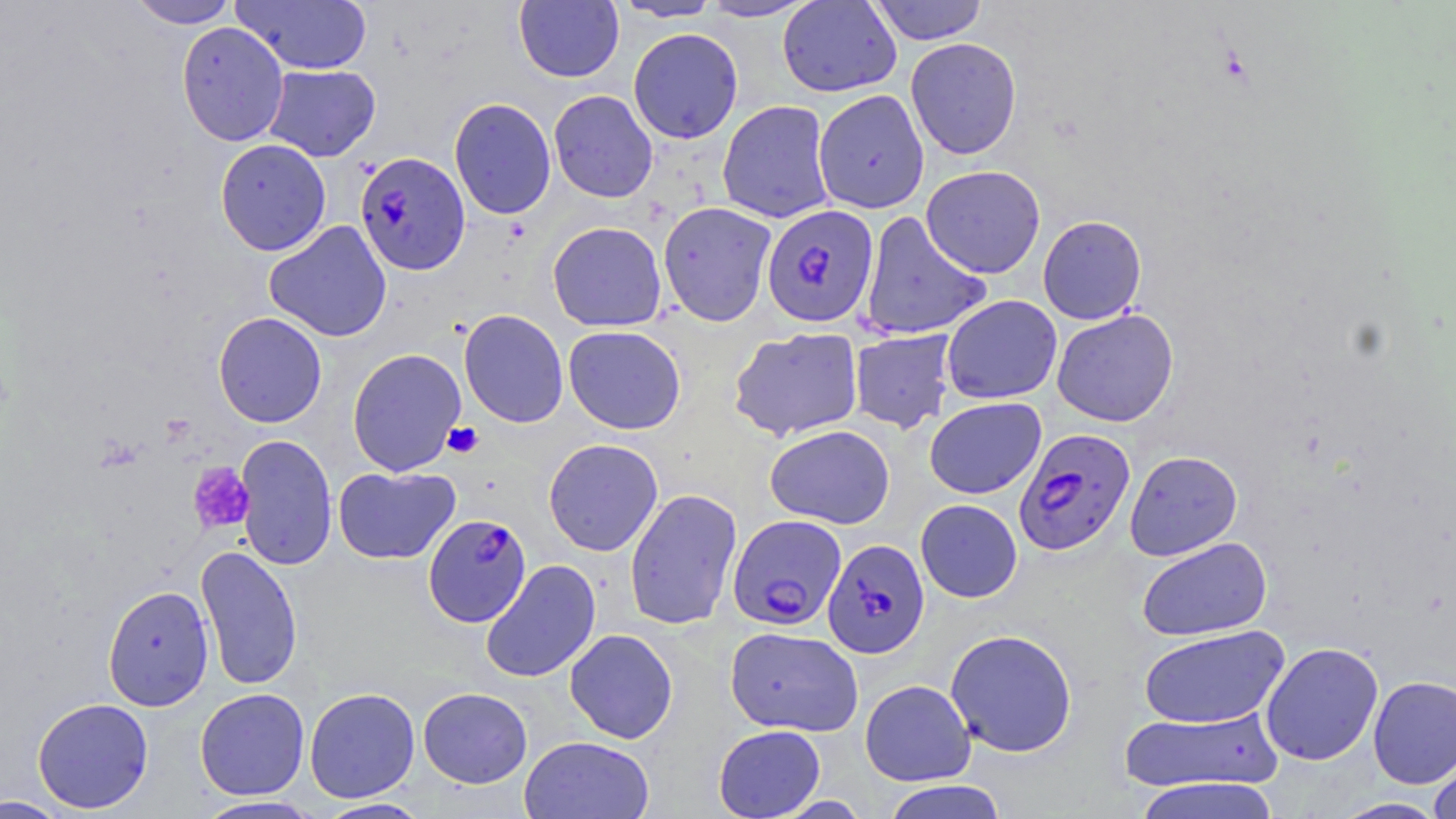
slide-level diagnosis = Plasmodium falciparum
magnification = 1000x
platelet locations = approximate bounding boxes as named x1/y1/x2/y2 corners in pixels: (x1=442, y1=422, x2=484, y2=458), (x1=188, y1=463, x2=255, y2=534)
Plasmodium falciparum-infected red blood cell locations = approximate bounding boxes as named x1/y1/x2/y2 corners in pixels: (x1=354, y1=150, x2=471, y2=275), (x1=761, y1=205, x2=880, y2=328), (x1=1013, y1=428, x2=1136, y2=556), (x1=423, y1=514, x2=531, y2=627), (x1=727, y1=514, x2=847, y2=632), (x1=823, y1=539, x2=930, y2=659)
field of view = one of a larger specimen
modality = light microscopy
uninfected red blood cell locations = approximate bounding boxes as named x1/y1/x2/y2 corners in pixels: (x1=127, y1=0, x2=239, y2=29), (x1=230, y1=0, x2=373, y2=75), (x1=514, y1=0, x2=624, y2=83), (x1=612, y1=0, x2=723, y2=22), (x1=776, y1=0, x2=901, y2=97), (x1=868, y1=0, x2=988, y2=45), (x1=696, y1=1, x2=819, y2=22), (x1=176, y1=21, x2=290, y2=146), (x1=628, y1=27, x2=743, y2=144), (x1=905, y1=37, x2=1022, y2=159), (x1=262, y1=64, x2=381, y2=161), (x1=813, y1=89, x2=930, y2=214), (x1=548, y1=90, x2=658, y2=203), (x1=448, y1=97, x2=557, y2=220), (x1=717, y1=100, x2=835, y2=224), (x1=214, y1=138, x2=331, y2=256), (x1=921, y1=164, x2=1045, y2=278), (x1=658, y1=201, x2=777, y2=326), (x1=858, y1=211, x2=992, y2=340), (x1=1037, y1=215, x2=1147, y2=325), (x1=263, y1=220, x2=392, y2=342), (x1=547, y1=221, x2=667, y2=332), (x1=941, y1=295, x2=1062, y2=404), (x1=1051, y1=308, x2=1179, y2=427), (x1=458, y1=309, x2=569, y2=428), (x1=213, y1=311, x2=327, y2=428), (x1=563, y1=325, x2=686, y2=434), (x1=729, y1=326, x2=864, y2=441), (x1=849, y1=329, x2=957, y2=434), (x1=347, y1=347, x2=467, y2=476), (x1=924, y1=396, x2=1046, y2=500), (x1=765, y1=424, x2=896, y2=529), (x1=234, y1=434, x2=338, y2=571), (x1=543, y1=437, x2=664, y2=556), (x1=1125, y1=450, x2=1243, y2=561), (x1=332, y1=465, x2=460, y2=564), (x1=624, y1=488, x2=742, y2=630), (x1=915, y1=499, x2=1023, y2=602), (x1=1137, y1=536, x2=1272, y2=641), (x1=195, y1=544, x2=303, y2=691), (x1=480, y1=559, x2=601, y2=683), (x1=102, y1=585, x2=214, y2=711), (x1=1139, y1=624, x2=1289, y2=728), (x1=725, y1=626, x2=864, y2=737), (x1=564, y1=628, x2=678, y2=743), (x1=945, y1=628, x2=1078, y2=757), (x1=1260, y1=641, x2=1383, y2=765), (x1=1368, y1=675, x2=1456, y2=788), (x1=859, y1=679, x2=975, y2=785), (x1=304, y1=687, x2=420, y2=803), (x1=418, y1=687, x2=532, y2=788), (x1=194, y1=688, x2=310, y2=800), (x1=32, y1=697, x2=154, y2=813), (x1=1120, y1=707, x2=1283, y2=793), (x1=713, y1=724, x2=826, y2=818), (x1=519, y1=735, x2=654, y2=819), (x1=1428, y1=752, x2=1456, y2=819), (x1=1131, y1=777, x2=1282, y2=819), (x1=880, y1=780, x2=1010, y2=819), (x1=0, y1=795, x2=74, y2=818), (x1=194, y1=796, x2=325, y2=818), (x1=316, y1=797, x2=433, y2=818), (x1=1331, y1=797, x2=1449, y2=818)
preparation = thin blood film
image size = 1456×819 pixels
stain = May-Grünwald-Giemsa